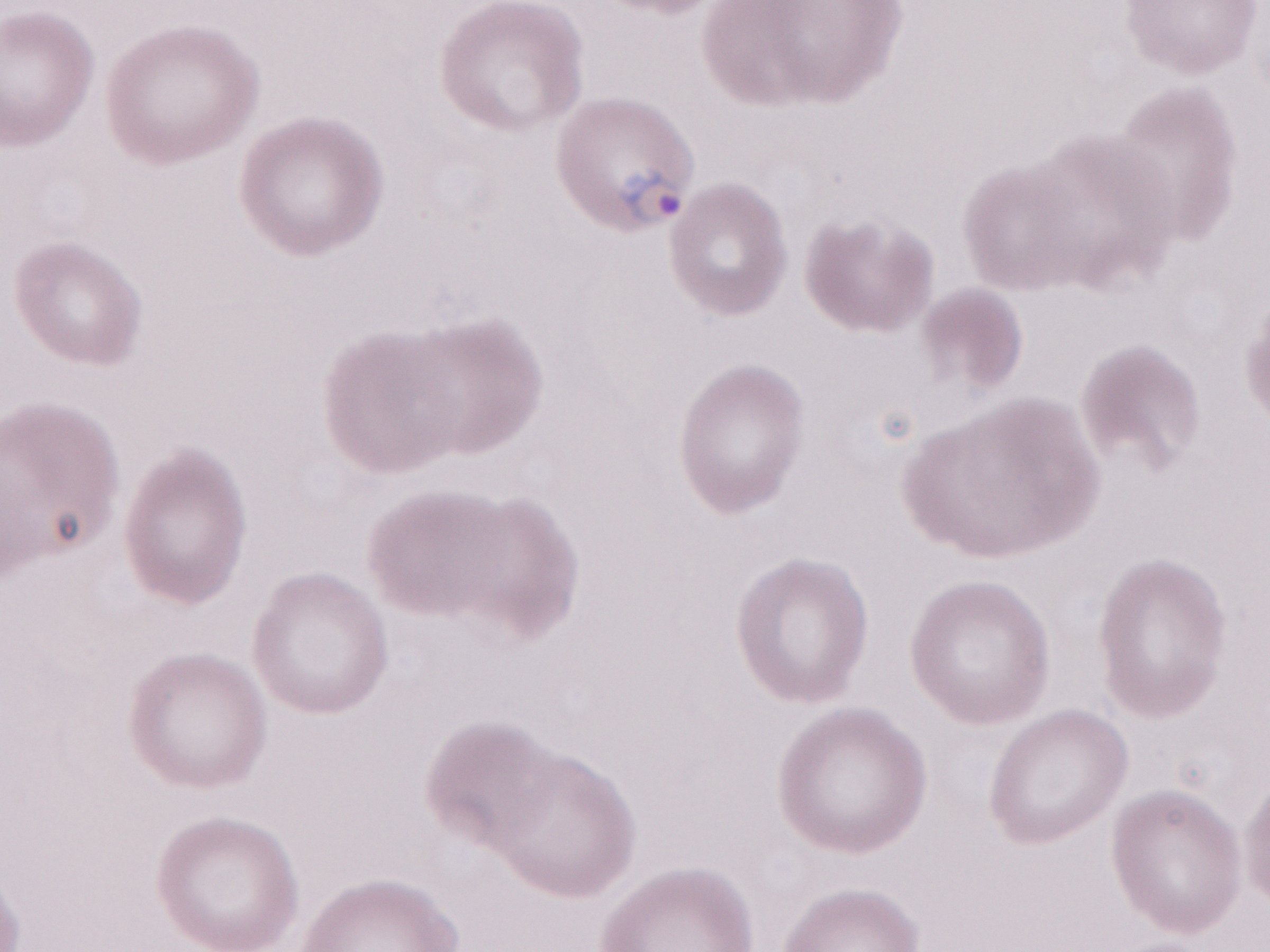 Image is 1270×952 pixels. Single field of view. Thin peripheral-blood smear. May-Grünwald-Giemsa-stained preparation. 1,000x magnification. Patient-level malaria diagnosis: positive. Olympus BX43 microscope and DP73 digital camera.